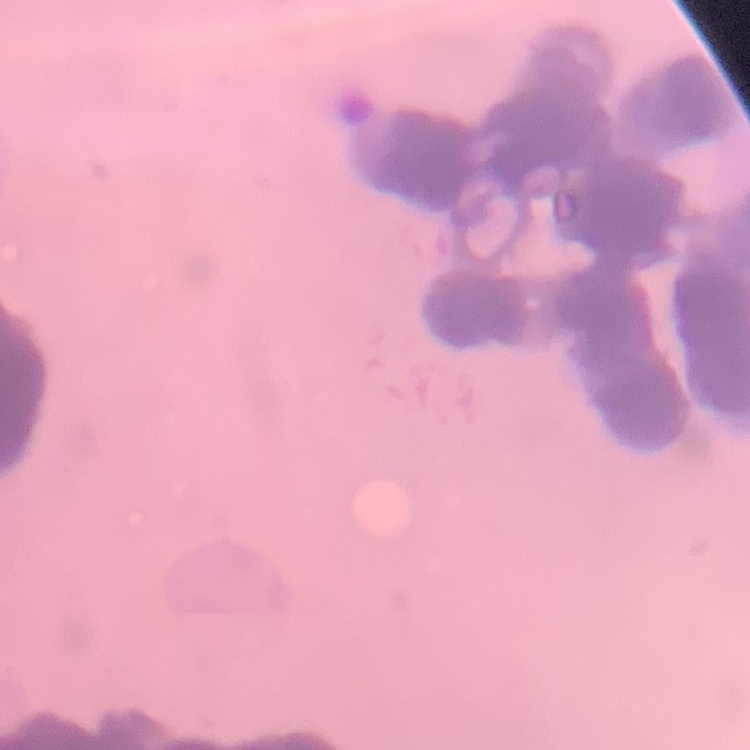
erythrocyte morphology = rouleaux formation
preparation = thin blood film
stain = Field's or Giemsa
image type = square crop of a larger photomicrograph